Comment on the morphology of the erythrocytes.
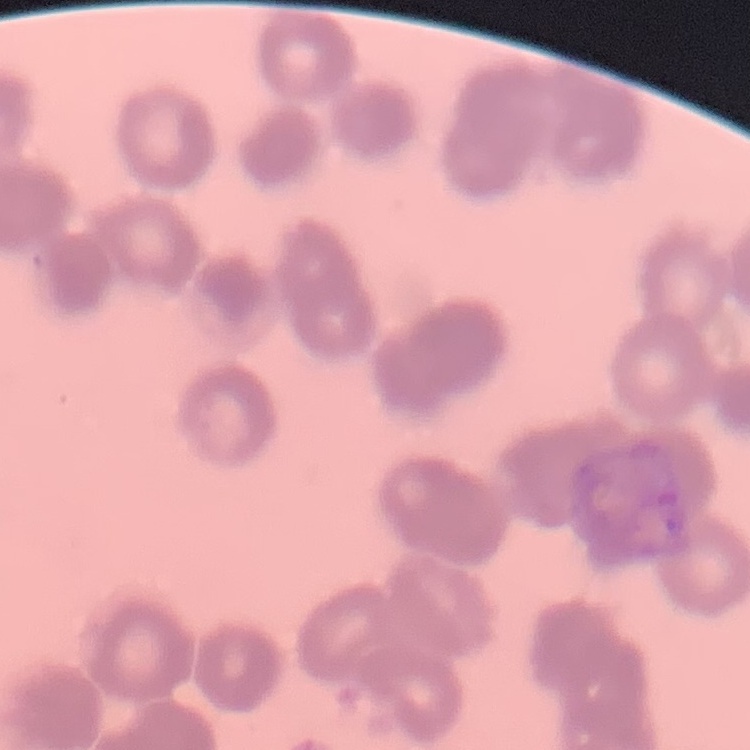
Rouleaux formation.

Thin blood film. Field's or Giemsa stain. Square crop of a larger photomicrograph.